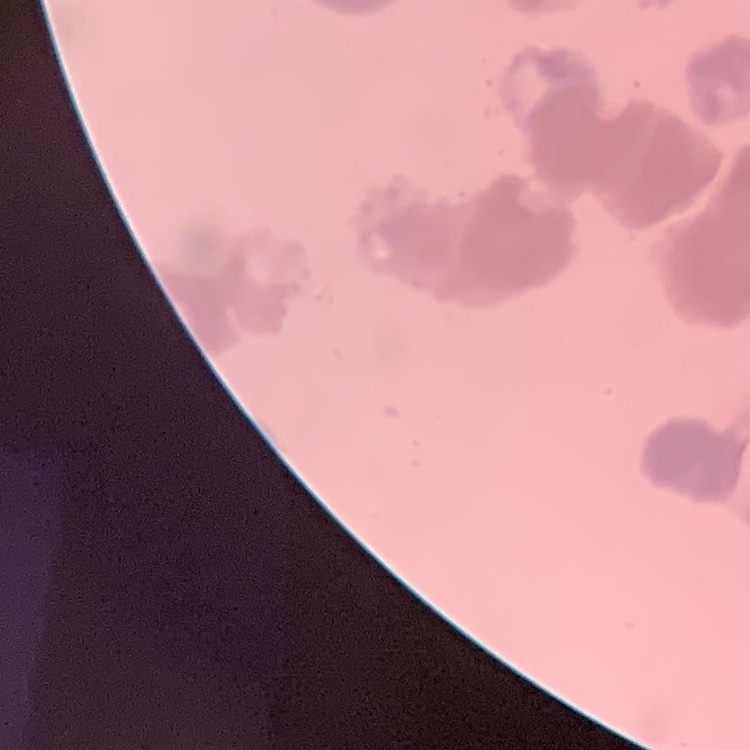

The red blood cells show rouleaux formation. Stained with either Field's or Giemsa. Square crop of a larger photomicrograph. Thin peripheral smear.